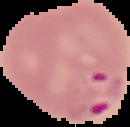
Summary:
  - Malaria status: parasitized
  - Image size: 130×127 pixels
  - Image type: segmented cell region on a black background
  - Preparation: thin blood film